Assess for malaria.
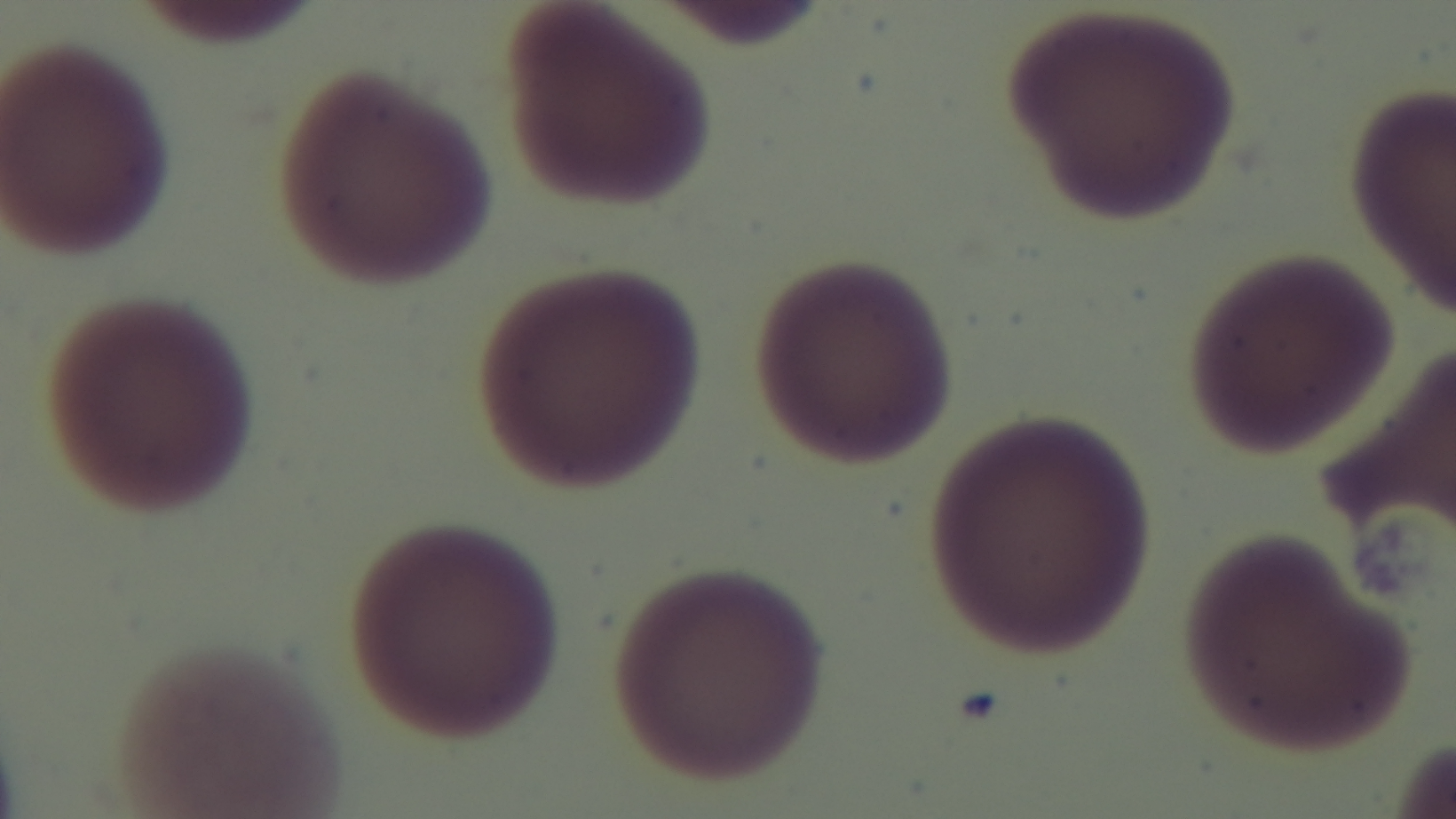
Negative.

Summary:
  - Preparation: thin
  - Capture: mounted 4K digital camera
  - Stain: Giemsa
  - Objective: 100x oil immersion
  - Modality: light microscopy
  - Field of view: one from the slide